State which parasite is depicted.
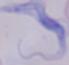

A trypanosome.

Photomicrograph. Captured at 1000x magnification.